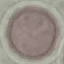
Malaria status: uninfected. Thin blood film. Giemsa-stained preparation. Acquired by smartphone through the microscope eyepiece. Automatically extracted cell patch, resized to 64 × 64 pixels.